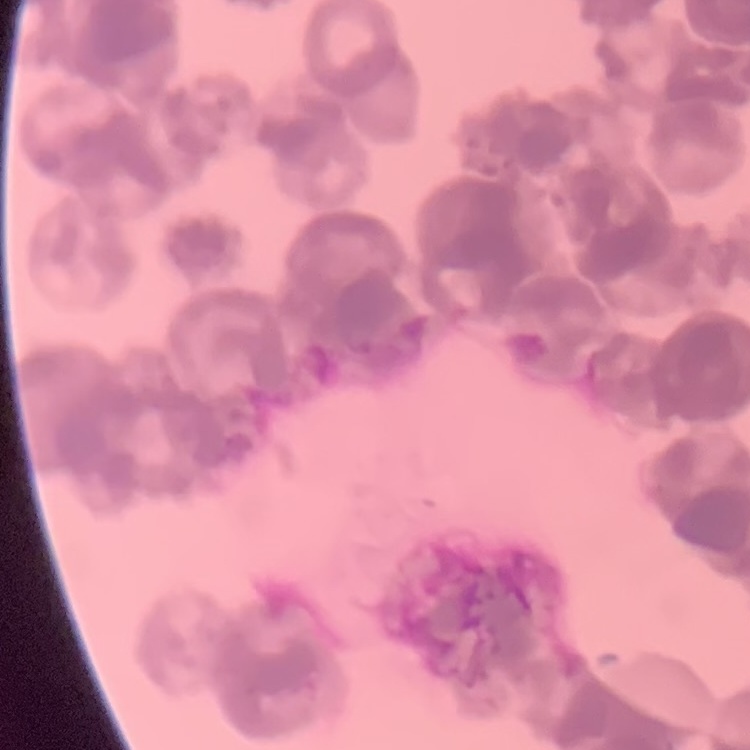
The red blood cells show rouleaux formation. Field's or Giemsa stain. Thin blood film. Square crop of a larger photomicrograph.